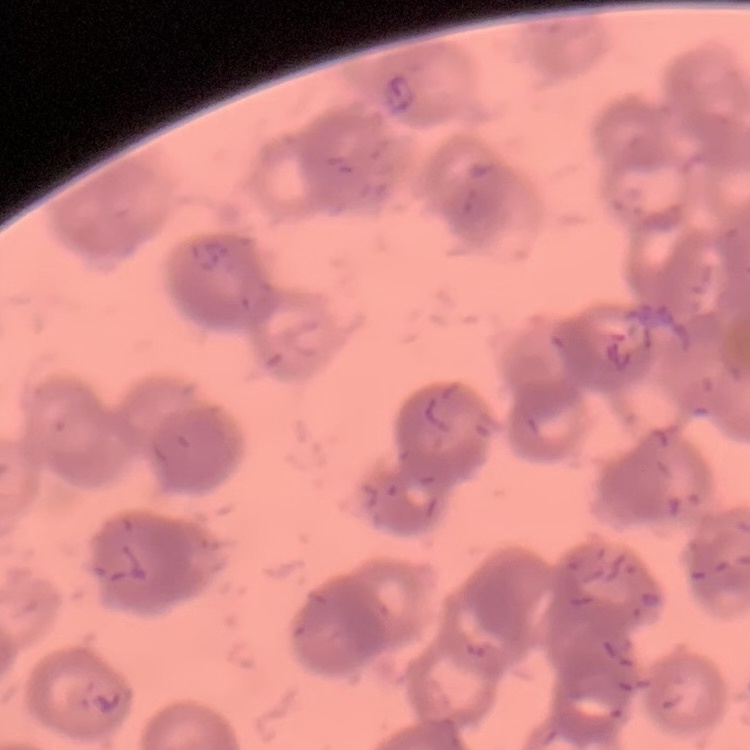
The erythrocytes exhibit rouleaux formation. Thin blood smear. One tile cut from a larger photomicrograph. Stained with either Field's or Giemsa.